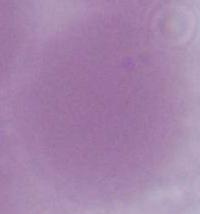

A red blood cell is seen. Micrograph. Captured at 1000x magnification.